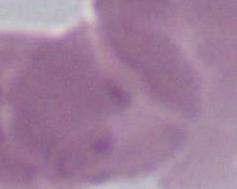
Summary:
  - Identification: erythrocyte
  - Magnification: 1000x
  - Modality: photomicrograph